Classify this cell by malaria status.
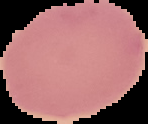
It is uninfected.

Image is 148×124 pixels. The area outside the segmented cell region is set to black. From a thin blood film.